Locate every leukocyte (white blood cell).
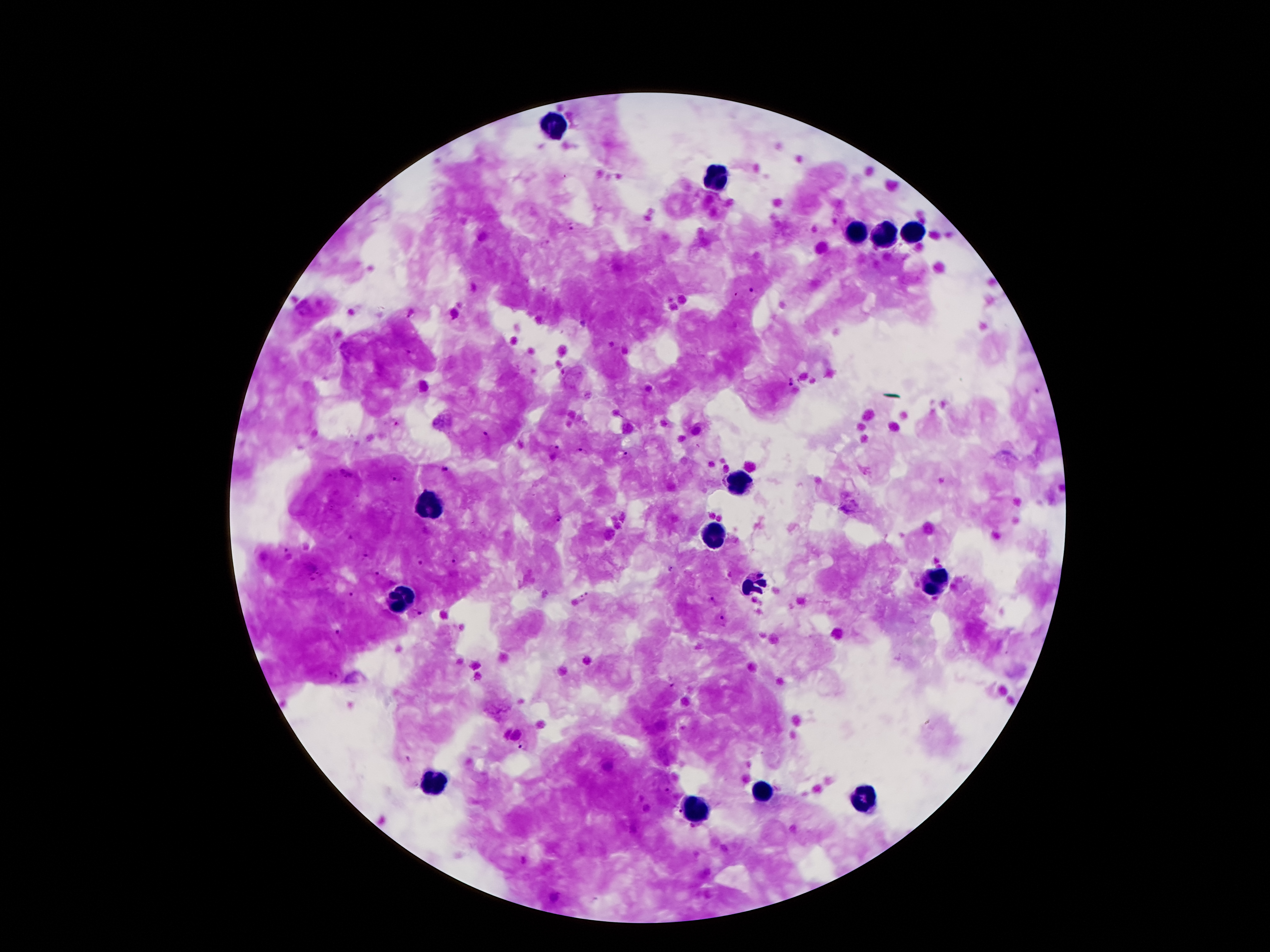

Approximate centers as [x, y] in pixels.
Leukocytes: [554, 126], [714, 180], [914, 230], [858, 234], [885, 235], [740, 487], [429, 503], [714, 537], [935, 582], [757, 583], [405, 600], [436, 782], [762, 794], [865, 801], [692, 811].

Malaria parasite locations: [571, 228], [546, 243], [752, 293], [411, 313], [455, 315], [410, 352], [794, 382], [397, 424], [487, 434], [558, 448], [580, 450], [626, 455], [444, 469], [346, 474], [396, 480], [559, 518], [350, 538], [287, 549], [365, 555], [421, 561], [455, 561], [672, 569], [378, 572], [312, 579], [355, 593], [712, 598], [584, 599], [417, 613], [722, 620], [340, 634], [333, 675], [673, 685], [524, 745], [667, 791], [676, 814]. 100x magnification. Giemsa-stained preparation. Thick blood smear. Smartphone photograph taken through the microscope eyepiece. Image is 1270×952 pixels. Single field of view. Patient malaria status: infected with Plasmodium falciparum.